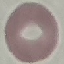 Result: negative for malaria parasites. Acquired by smartphone through the microscope eyepiece. Giemsa stain. Thin smear of blood. Automatically extracted cell patch, resized to 64 × 64 pixels.